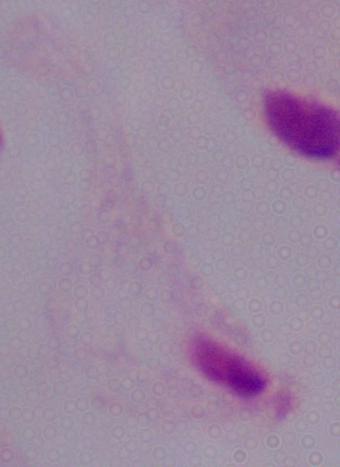
{
  "identification": "trichomonad",
  "magnification": "1000x",
  "modality": "photomicrograph"
}